Report the malaria status of this cell.
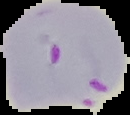
It is parasitized.

Summary:
  - Image size: 130×115 pixels
  - Preparation: thin blood smear
  - Image type: segmented cell region on a black background